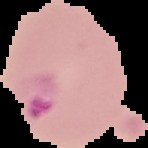

Summary:
  - Malaria status: parasitized
  - Image type: segmented cell region on a black background
  - Preparation: thin blood smear
  - Image size: 148×148 pixels